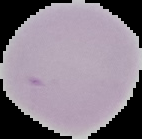

Cell region segmented out of the field of view; the surrounding area is masked to black. Image is 142×139 pixels. From a thin blood film. Result: negative for malaria parasites.